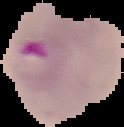

preparation: thin blood film
result: Plasmodium parasites detected
image_size: 124×127 pixels
image_type: segmented cell region with the area outside set to black